Locate every malaria parasite.
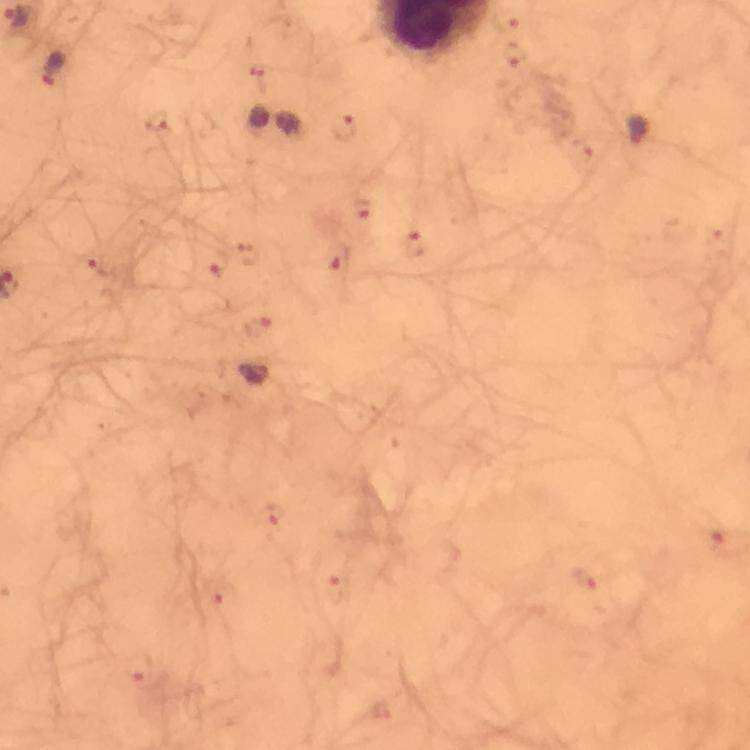

Approximate object centers, in pixels from the top-left corner.
Malaria parasites: (x=505, y=18), (x=515, y=54), (x=53, y=68), (x=158, y=120), (x=344, y=127), (x=363, y=208), (x=414, y=245), (x=337, y=257), (x=217, y=262), (x=89, y=264), (x=258, y=327), (x=271, y=514), (x=584, y=579), (x=335, y=588), (x=216, y=591), (x=138, y=669).

Image is 750×750 pixels. Thick smear. Giemsa stain. Cropped region of a single field of view. Photographed through the microscope with a smartphone camera. From a diagnostic examination for malaria. Immersion oil applied. At 100x magnification.